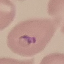

Summary:
  - Result: malaria parasites identified
  - Stain: Giemsa
  - Capture: smartphone camera at the microscope eyepiece
  - Image type: automatically extracted cell patch, resized to 64 × 64 pixels
  - Preparation: thin smear